Identify the cell.
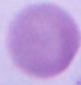
This is an erythrocyte.

Micrograph. Captured at 1000x magnification.